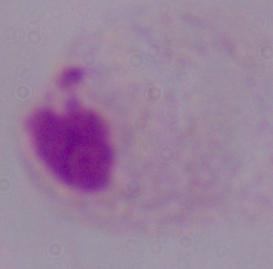
A trichomonad is shown. Captured at 1000x magnification. Photomicrograph.